Report the malaria status of this cell.
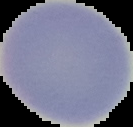
Uninfected.

Summary:
  - Preparation: thin blood film
  - Image type: cell region segmented out of the field of view; surrounding area masked to black
  - Image size: 133×127 pixels